Classify this cell by malaria status.
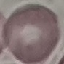

Uninfected.

{
  "image_type": "cell patch, automatically extracted from a larger field of view and resized to 64 × 64 pixels",
  "capture": "smartphone through the microscope eyepiece",
  "stain": "Giemsa",
  "preparation": "thin blood smear"
}